Identify the parasite.
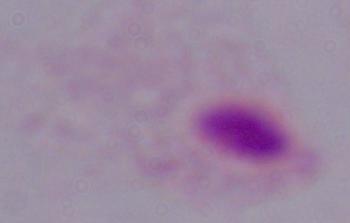
This is a trichomonad.

magnification: 1000x
modality: photomicrograph